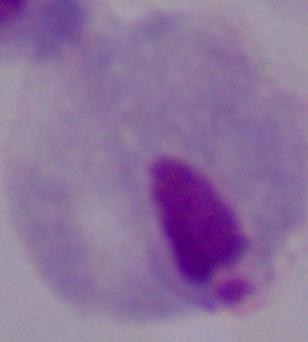
modality: photomicrograph
magnification: 1000x
identification: trichomonad